Give the position of every malaria parasite.
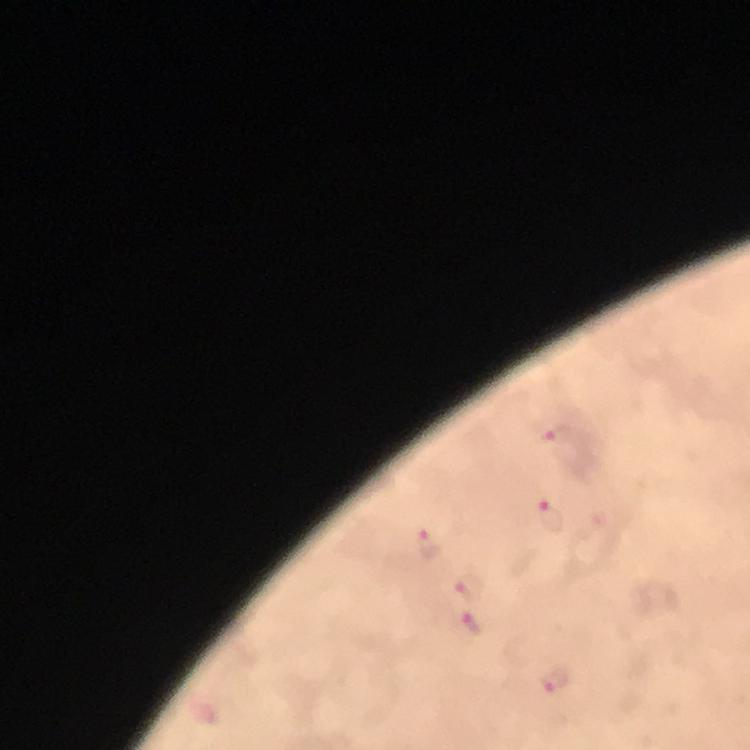
Approximate centers as (x, y) in pixels.
Malaria parasites: (556, 438), (552, 515), (430, 542), (470, 587), (473, 623), (557, 679).

{
  "stain": "Giemsa",
  "preparation": "thick blood smear",
  "image_size": "750×750 pixels",
  "cropped_from": "one field of view",
  "immersion_oil": "applied",
  "magnification": "100x",
  "context": "from a diagnostic examination for malaria",
  "capture": "smartphone photograph through a microscope"
}